Identify the parasite.
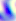
Toxoplasma gondii.

Captured at 400x magnification. Micrograph.